Describe the morphology of the erythrocytes.
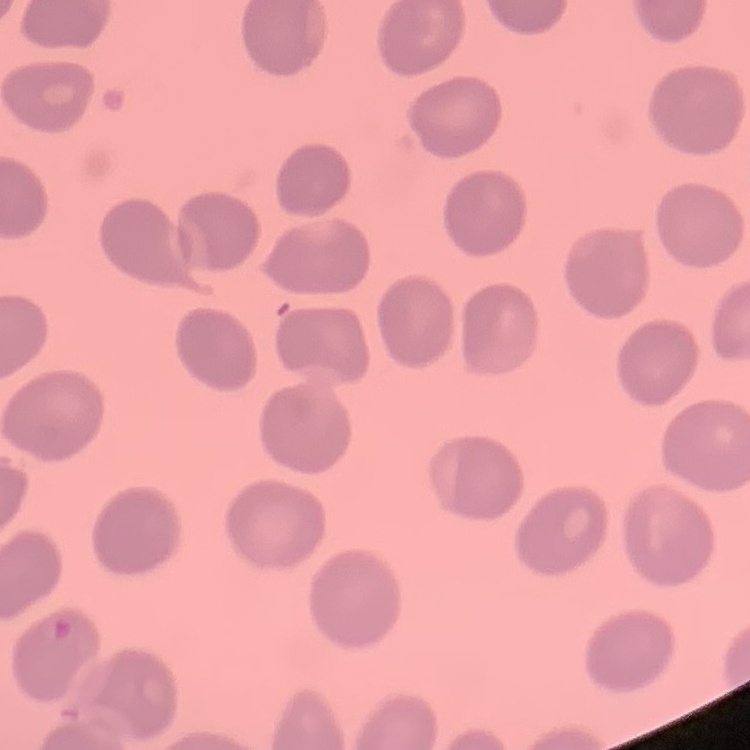
No rouleaux formation.

preparation = thin peripheral smear
image type = square crop of a larger photomicrograph
stain = Field's or Giemsa